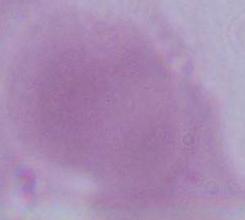

A red blood cell is shown. Micrograph. 1000x magnification.